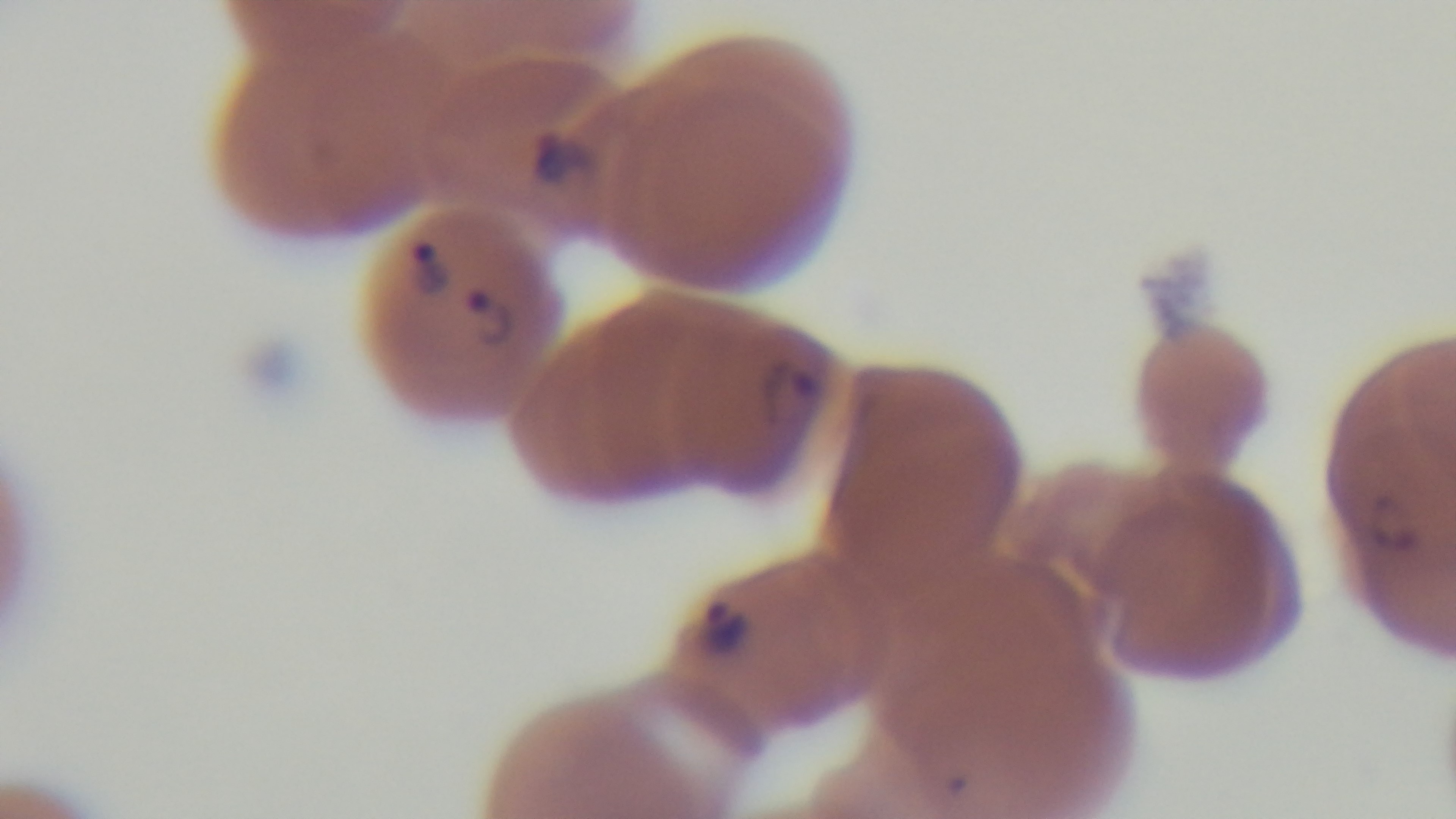
malaria status = positive
modality = light microscopy
field of view = one from the slide
capture = mounted 4K digital camera
stain = Giemsa
preparation = thin smear
objective = 100x oil immersion